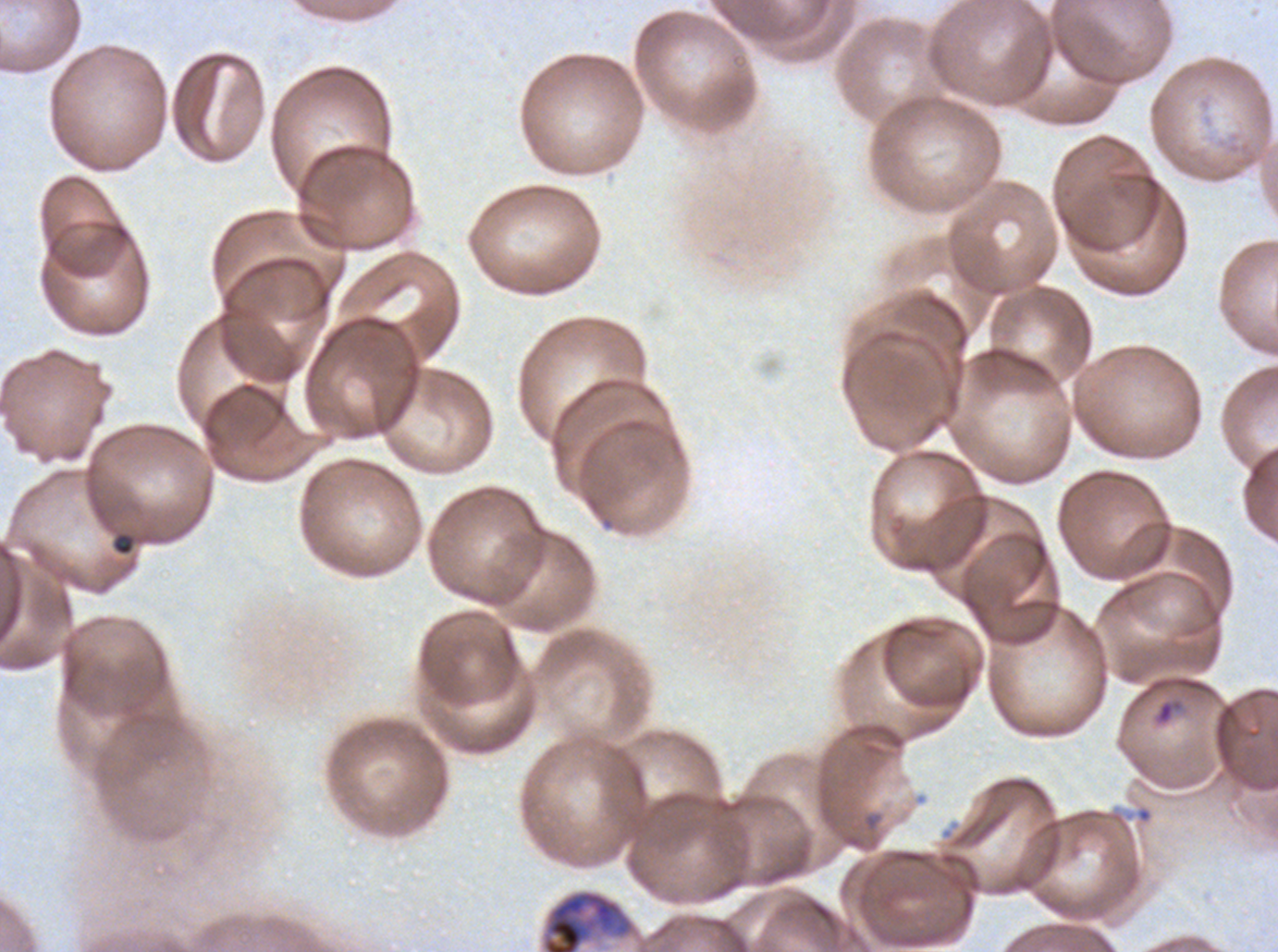
Approximate bounding boxes as {x1, y1, x2, y2} in pixels. Debris locations: {112, 532, 135, 556}. Ring locations: {1157, 701, 1174, 723}. Late schizont locations: {541, 889, 636, 951}. Giemsa-stained preparation. Image is 1278×952 pixels. Life-cycle stages observed: ring, late schizont. Thin blood film. One sub-image of a larger composite. Plasmodium falciparum cultured ex vivo for 24 to 48 hours, from a patient in The Gambia.